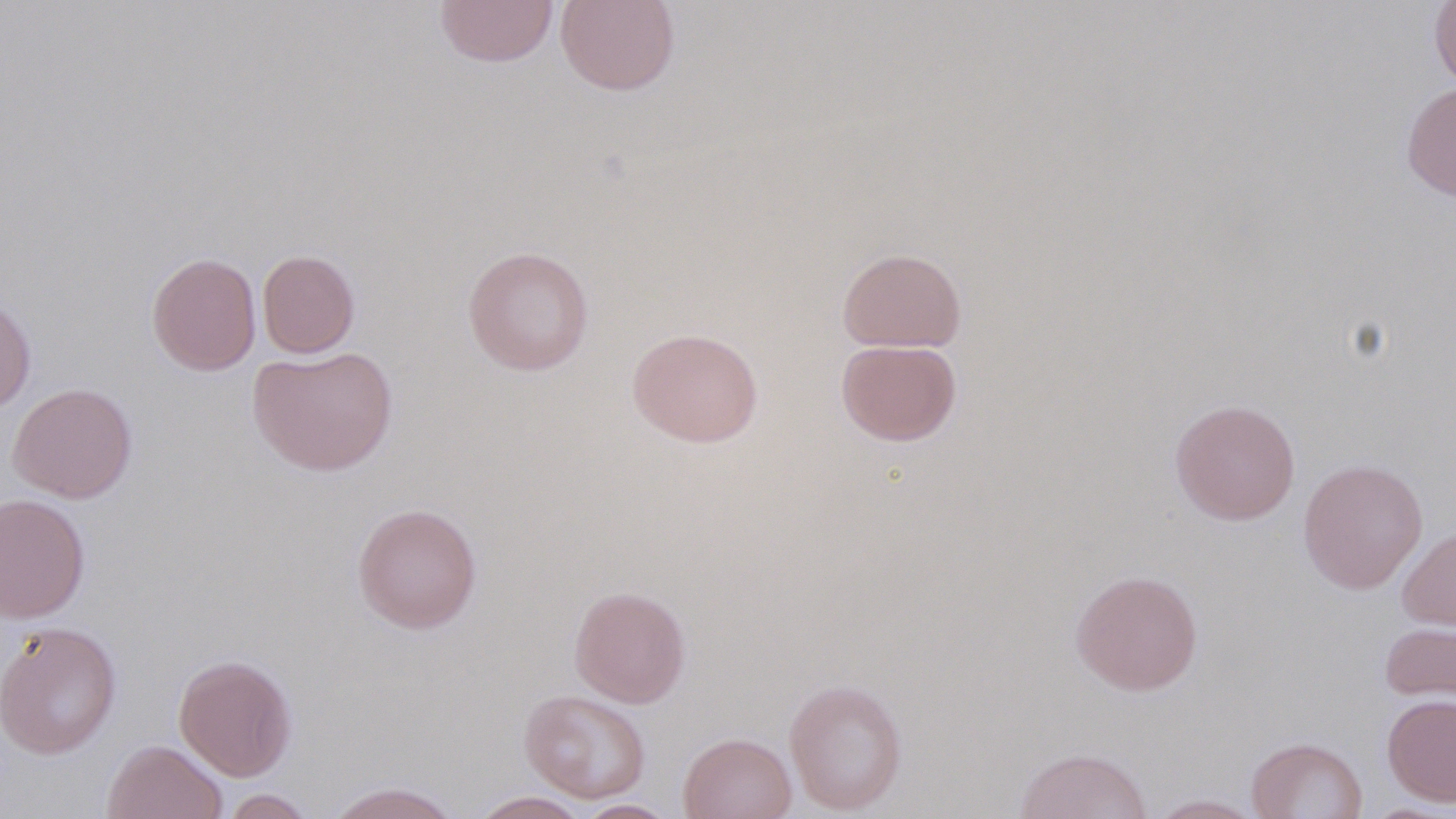
Approximate bounding boxes as (x1,y1)-(x2,y2) corner pairs in pixels. Uninfected red blood cell locations: (434,0)-(559,67), (555,0)-(681,96), (1429,0)-(1456,92), (1401,82)-(1456,203), (462,245)-(594,376), (837,247)-(966,353), (257,250)-(360,358), (146,251)-(262,376), (0,296)-(36,413), (626,327)-(764,448), (835,339)-(962,447), (248,346)-(398,476), (8,382)-(138,504), (1169,398)-(1301,525), (1297,458)-(1428,594), (0,493)-(90,623), (352,502)-(482,634), (1397,525)-(1455,633), (1070,569)-(1203,696), (569,585)-(691,708), (1379,620)-(1456,708), (0,621)-(122,760), (173,654)-(298,781), (784,677)-(908,815), (519,689)-(651,803), (1381,694)-(1456,807), (678,732)-(796,819), (1246,737)-(1368,819), (102,739)-(228,819), (1013,746)-(1153,819), (324,781)-(463,819), (219,789)-(317,818), (469,791)-(591,818), (1146,794)-(1266,818), (575,799)-(677,818), (1360,802)-(1455,818). Slide-level diagnosis: no evidence of blood parasites. Captured at 1000x magnification. Optical microscopy. May-Grünwald-Giemsa-stained preparation. Image is 1456×819 pixels. Thin blood film. One field of a larger specimen.